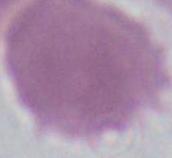 Photomicrograph. An erythrocyte is shown. 1000x magnification.